Describe the morphology of the erythrocytes.
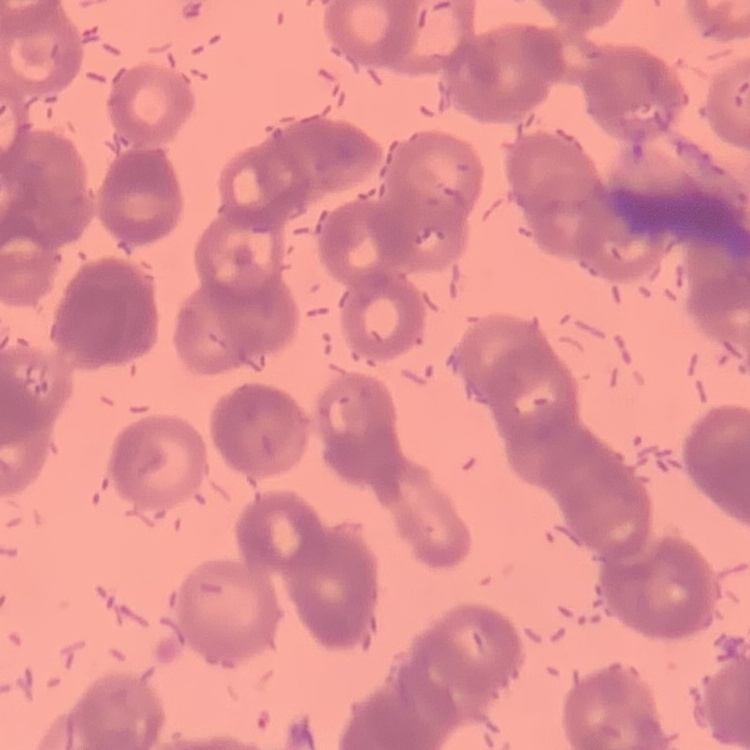
They show rouleaux formation.

Summary:
  - Stain: Field's or Giemsa
  - Image type: one tile cut from a larger photomicrograph
  - Preparation: thin blood film